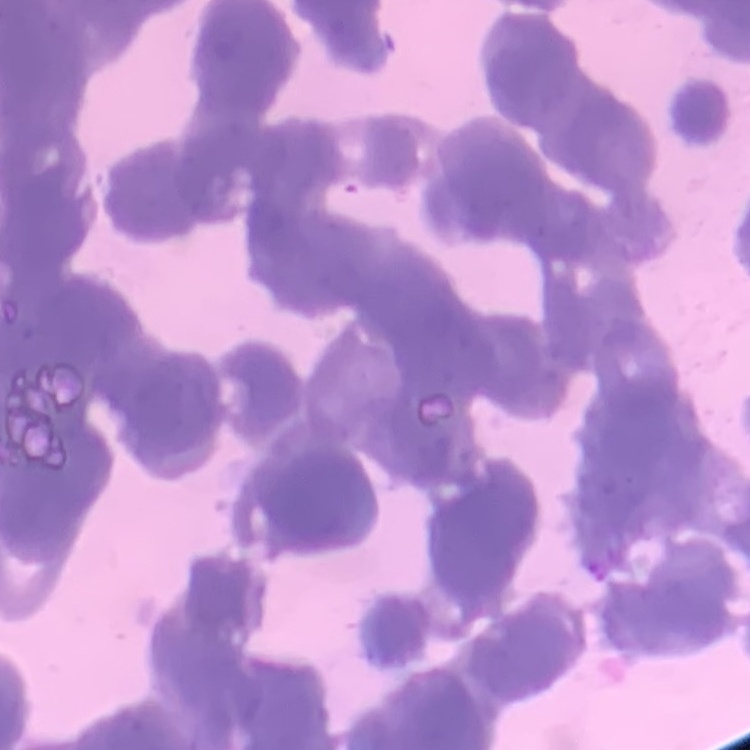

Summary:
  - Erythrocyte morphology: rouleaux formation
  - Image type: square crop of a larger photomicrograph
  - Stain: Field's or Giemsa
  - Preparation: thin peripheral smear